Name the parasite shown.
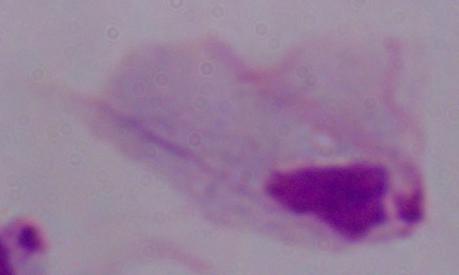

This is a trichomonad.

magnification: 1000x
modality: micrograph